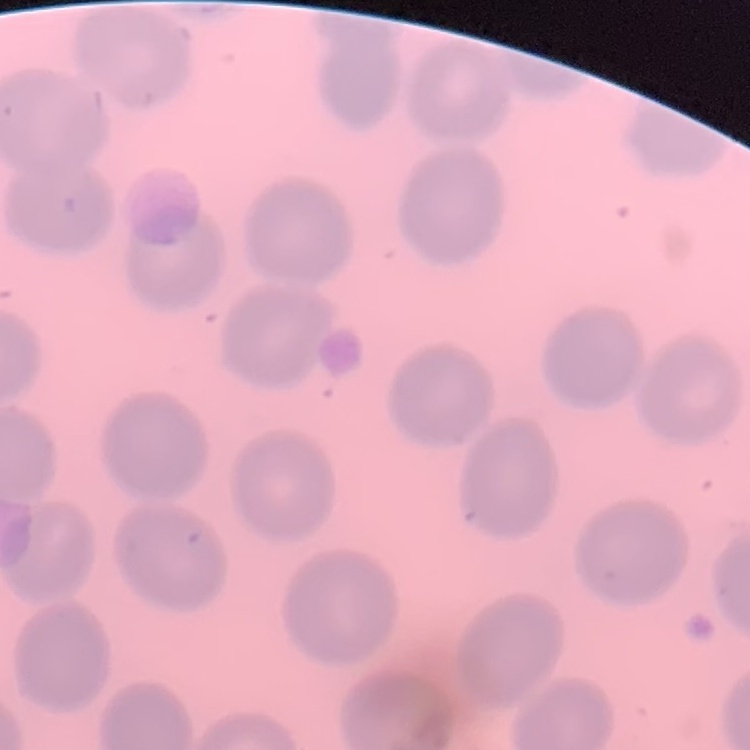

Summary:
  - Erythrocyte morphology: no rouleaux formation
  - Image type: square crop of a larger photomicrograph
  - Preparation: thin peripheral smear
  - Stain: Field's or Giemsa